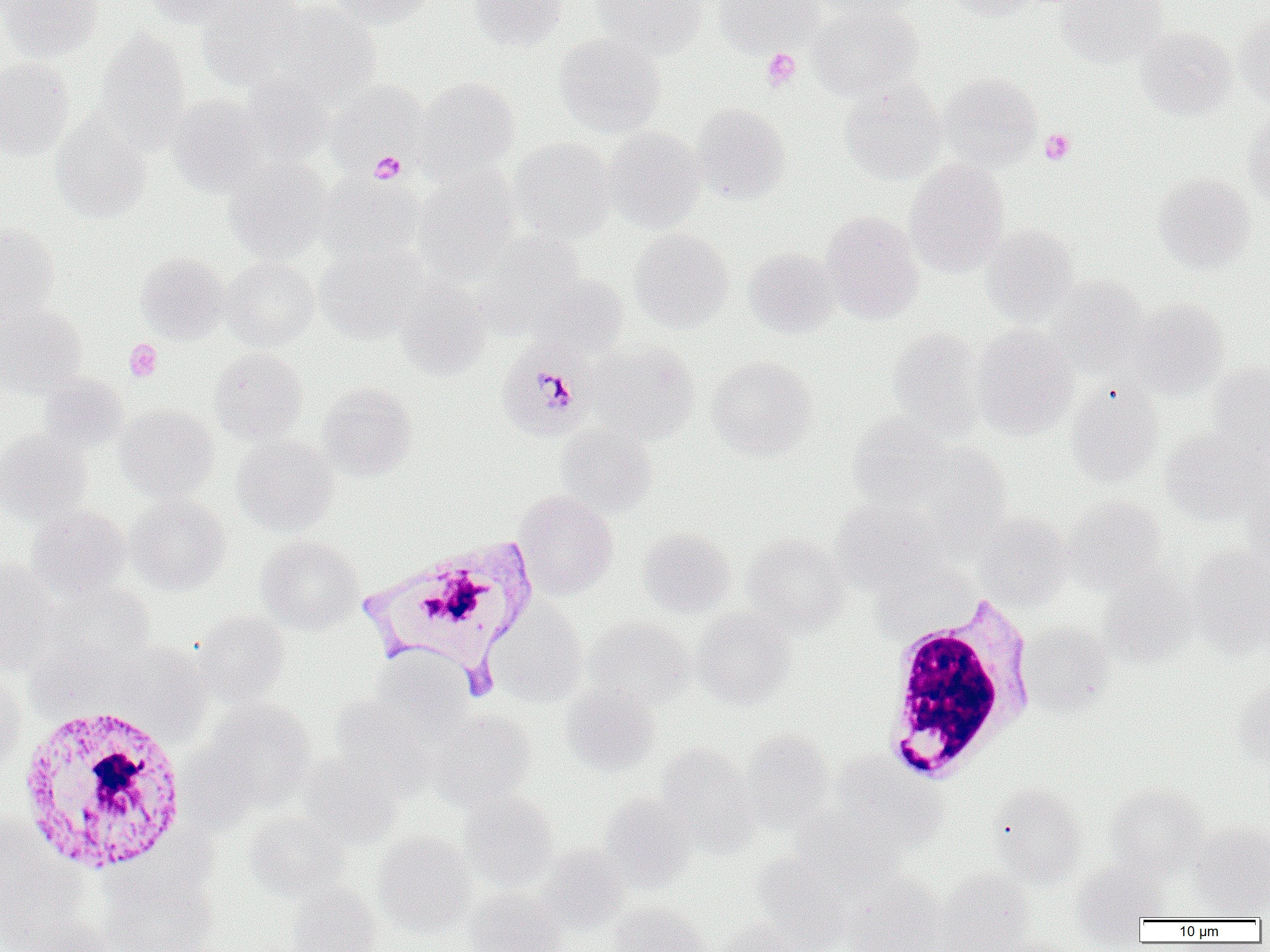
Summary:
  - Coordinate format: approximate bounding boxes as (x1,y1)-(x2,y2) corner pairs in pixels
  - Platelet locations: (761,47)-(801,91), (1039,128)-(1075,164), (369,151)-(406,184), (125,338)-(162,382)
  - White blood cell locations: (358,537)-(540,694), (879,596)-(1037,784), (16,704)-(191,876)
  - Plasmodium malariae-infected red blood cell locations: (501,347)-(595,442)
  - Uninfected red blood cell locations: (0,0)-(103,62), (146,0)-(250,28), (197,0)-(307,89), (326,0)-(437,27), (470,0)-(568,50), (592,0)-(710,58), (714,0)-(822,55), (811,0)-(923,20), (943,0)-(1038,21), (1055,0)-(1169,67), (264,2)-(383,105), (807,3)-(923,100), (1235,16)-(1270,107), (1135,26)-(1236,120), (94,28)-(191,149), (555,33)-(666,137), (0,57)-(74,160), (938,72)-(1042,170), (240,73)-(336,166), (416,76)-(519,177), (327,80)-(426,173), (840,80)-(946,184), (168,94)-(269,195), (691,103)-(790,203), (1243,107)-(1270,205), (50,114)-(153,223), (602,127)-(705,232), (509,138)-(616,241), (905,158)-(1009,276), (224,159)-(332,261), (414,165)-(520,282), (1153,173)-(1256,273), (318,174)-(425,265), (822,211)-(923,323), (0,223)-(60,321), (982,224)-(1078,324), (629,228)-(733,332), (474,229)-(584,333), (315,244)-(427,343), (743,247)-(839,338), (136,252)-(229,343), (221,256)-(320,351), (531,273)-(628,361), (1045,276)-(1148,377), (396,279)-(492,378), (1129,298)-(1229,398), (0,303)-(86,397), (972,324)-(1078,438), (888,328)-(986,437), (588,342)-(700,444), (209,348)-(308,443), (707,355)-(817,461), (1207,360)-(1270,454), (38,373)-(128,453), (316,383)-(418,480), (1066,383)-(1163,486), (116,404)-(218,501), (848,413)-(951,509), (556,424)-(657,517), (1162,425)-(1270,524), (0,430)-(90,524), (232,434)-(338,536), (911,442)-(1011,540), (1240,488)-(1270,577), (514,490)-(617,599), (126,494)-(230,594), (1062,495)-(1167,594), (831,498)-(948,592), (26,505)-(131,601), (974,514)-(1071,608), (637,527)-(735,619), (742,533)-(850,635), (256,535)-(363,634), (1186,544)-(1270,656), (0,559)-(64,672), (1099,570)-(1199,667), (45,581)-(155,664), (490,599)-(588,706), (692,608)-(796,708), (192,611)-(291,708), (586,617)-(696,709), (1019,622)-(1113,715), (25,639)-(139,718), (114,642)-(211,736), (369,650)-(475,743), (0,675)-(27,777), (1235,681)-(1270,773), (562,684)-(661,775), (331,695)-(438,797), (204,699)-(317,810), (431,709)-(536,808), (739,730)-(834,833), (655,743)-(758,850), (831,753)-(948,853), (296,755)-(403,848), (989,784)-(1088,888), (1104,784)-(1208,879), (458,792)-(559,890), (599,793)-(696,890), (790,806)-(904,891), (244,813)-(349,901), (0,820)-(82,946), (1189,821)-(1270,917), (373,831)-(477,936), (537,844)-(629,931), (751,852)-(852,949), (1071,864)-(1164,943), (935,867)-(1035,952), (100,874)-(218,952), (843,876)-(948,952), (286,883)-(382,952), (466,889)-(566,952), (608,903)-(708,952), (10,918)-(117,952), (716,920)-(798,952), (981,934)-(1076,952)
  - Slide-level diagnosis: Plasmodium malariae
  - Field of view: one of a larger specimen
  - Magnification: 1000x
  - Modality: optical microscopy
  - Preparation: thin blood film
  - Image size: 1270×952 pixels